Classify this cell by malaria status.
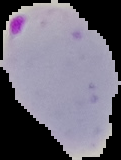

Parasitized.

image size = 121×160 pixels
image type = cell region segmented out of the field of view; surrounding area masked to black
preparation = thin blood smear